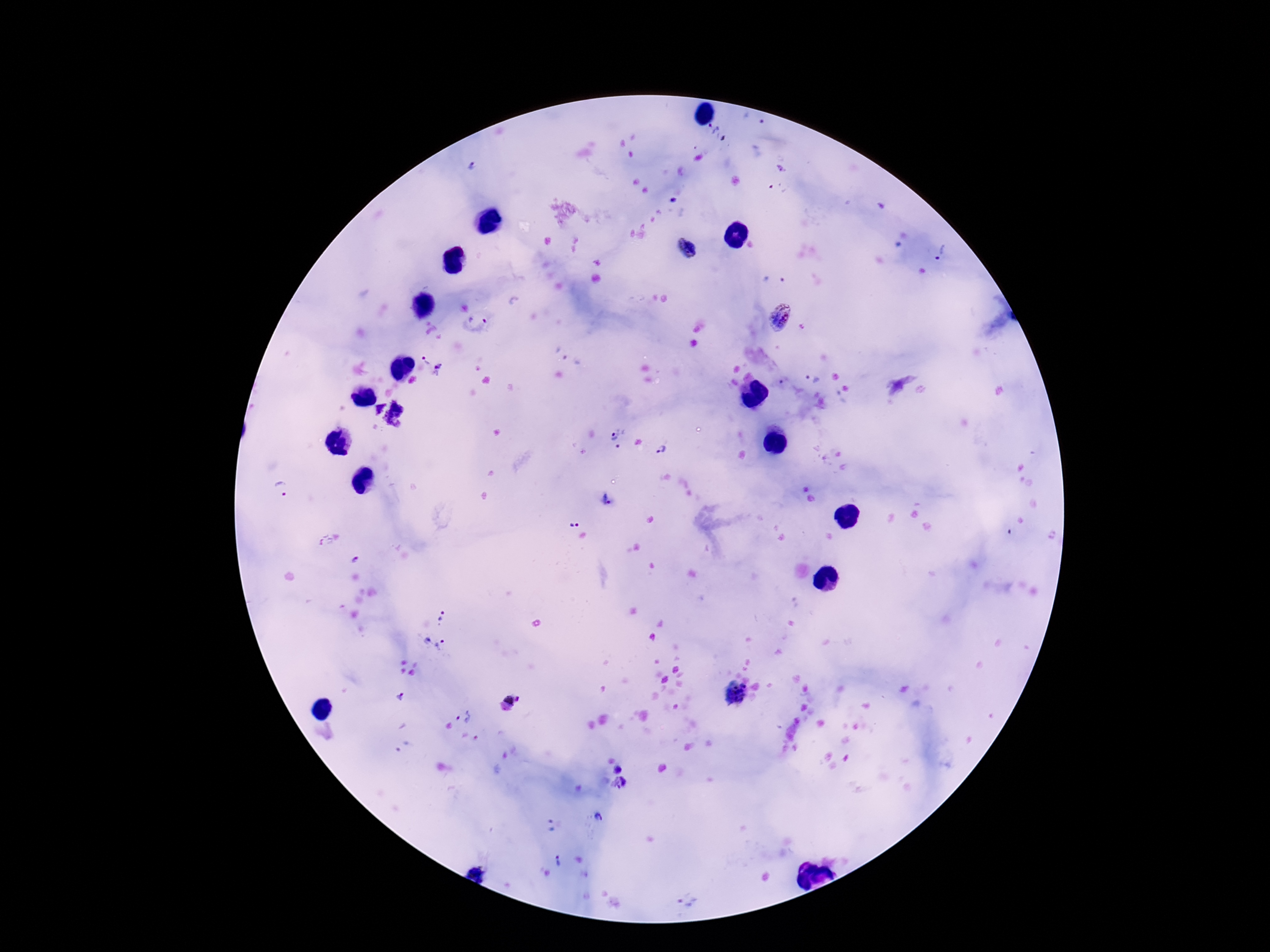 Approximate object centers, in pixels from the top-left corner. Plasmodium parasite locations: (x=713, y=128), (x=474, y=168), (x=687, y=250), (x=941, y=252), (x=774, y=278), (x=781, y=317), (x=476, y=324), (x=427, y=360), (x=441, y=369), (x=812, y=378), (x=839, y=399), (x=387, y=412), (x=614, y=430), (x=662, y=450), (x=281, y=492), (x=605, y=499), (x=575, y=523), (x=442, y=616), (x=433, y=641), (x=734, y=692), (x=401, y=696), (x=507, y=699), (x=518, y=699), (x=464, y=716), (x=620, y=768), (x=620, y=784), (x=599, y=817), (x=550, y=825), (x=557, y=862), (x=686, y=902). Giemsa stain. 100x magnification. One field from this slide. Patient malaria status: infected. Photographed through the microscope eyepiece with a smartphone camera. Thick peripheral-blood smear. Image is 1270×952 pixels.